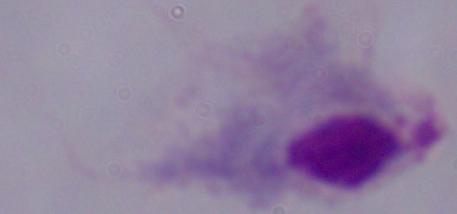 Micrograph. 1000x magnification. A trichomonad is seen.